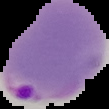

From a thin blood smear. Malaria status: parasitized. Image is 109×109 pixels. The area outside the segmented cell region is set to black.